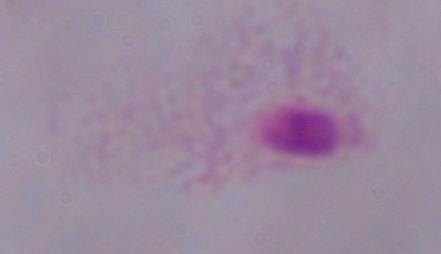
Summary:
  - Identification: trichomonad
  - Magnification: 1000x
  - Modality: micrograph